Comment on the morphology of the erythrocytes.
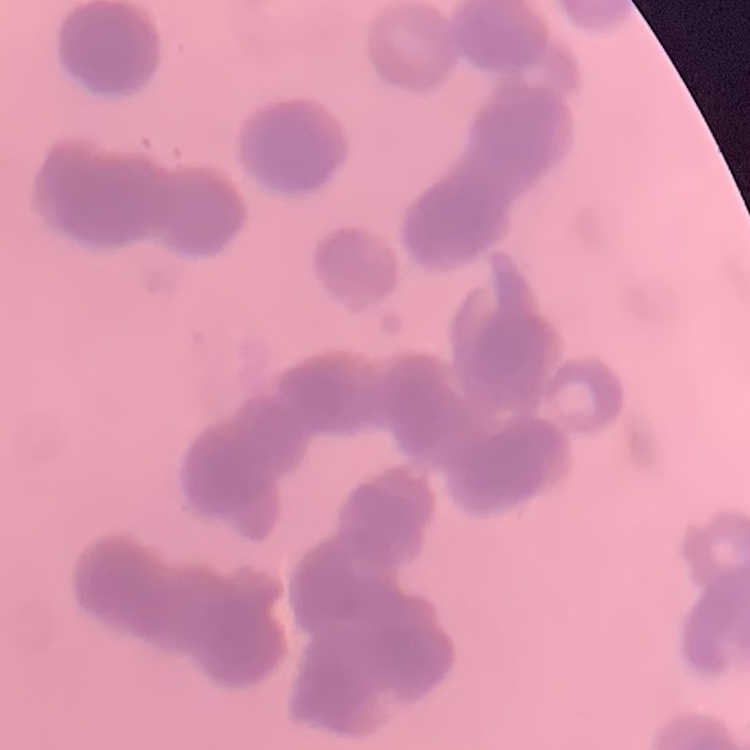

They show rouleaux formation.

preparation = thin peripheral smear
stain = Field's or Giemsa
image type = square crop of a larger photomicrograph